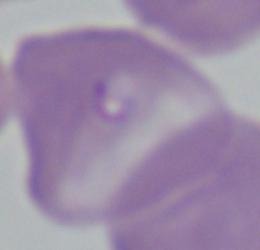

identification = Babesia
modality = photomicrograph
magnification = 1000x